Report the malaria status of this cell.
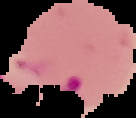
Parasitized.

From a thin blood film. Cell region segmented out of the field of view; the surrounding area is masked to black. Image is 136×118 pixels.